Assess this cell for malaria.
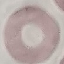

It is uninfected.

Thin blood film. Giemsa-stained preparation. Automatically extracted cell patch, resized to 64 × 64 pixels. Acquired by smartphone through the microscope eyepiece.